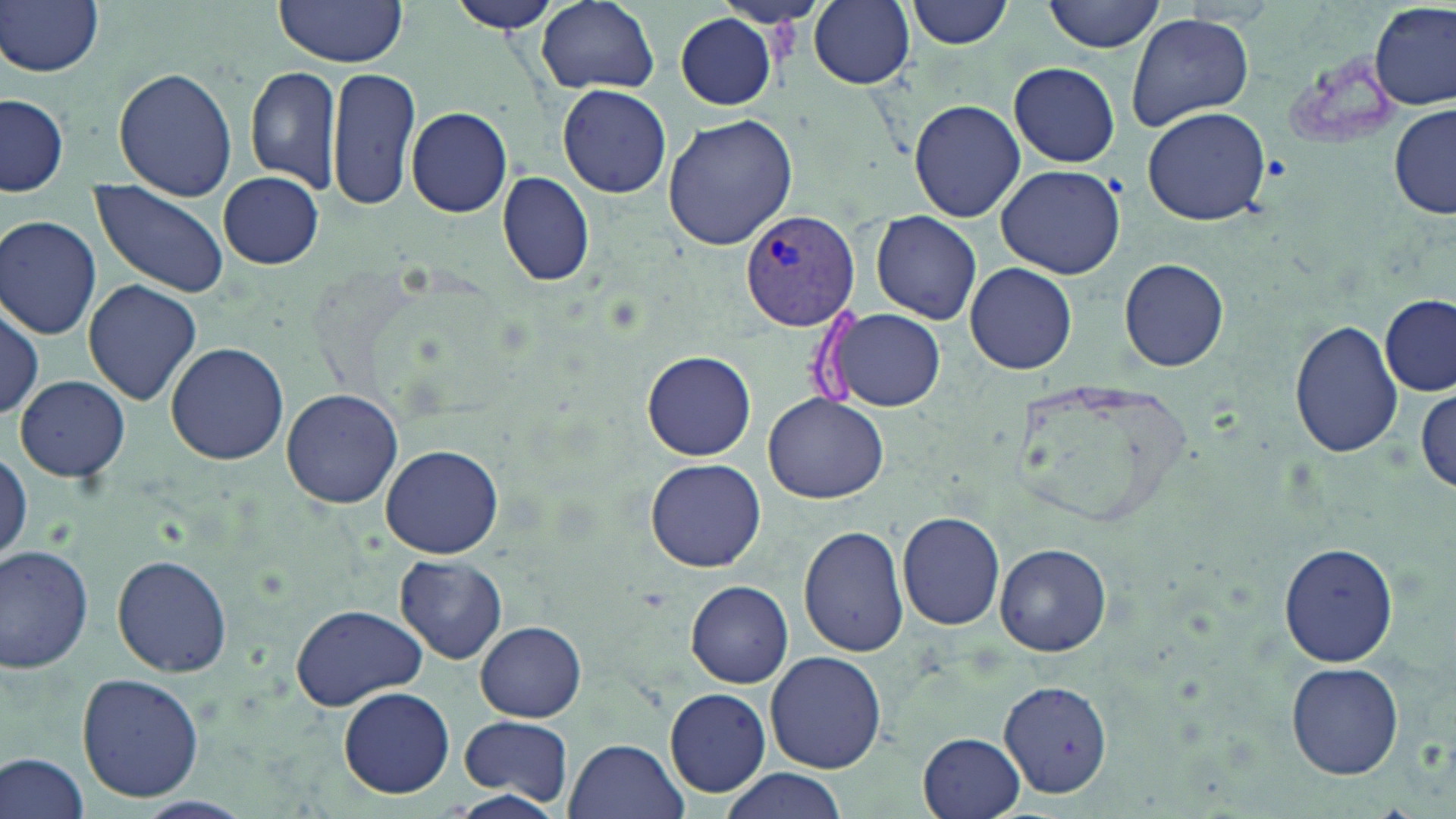
Summary:
  - Coordinate format: approximate bounding boxes as (x1,y1)-(x2,y2) corner pairs in pixels
  - Plasmodium vivax-infected red blood cell locations: (739,213)-(856,331)
  - Uninfected red blood cell locations: (271,0)-(409,69), (444,0)-(566,34), (536,0)-(660,94), (808,0)-(915,89), (906,0)-(1015,48), (1044,0)-(1166,51), (1,1)-(106,77), (1371,3)-(1454,112), (1127,12)-(1255,131), (676,13)-(776,110), (1008,62)-(1120,167), (114,65)-(237,201), (246,66)-(342,190), (328,66)-(422,213), (558,84)-(671,199), (1,92)-(70,194), (909,98)-(1026,222), (1140,105)-(1272,226), (1390,105)-(1456,221), (406,106)-(514,218), (662,113)-(799,251), (995,164)-(1126,279), (217,171)-(324,268), (495,172)-(596,287), (90,181)-(230,297), (868,213)-(987,324), (0,214)-(103,338), (1119,256)-(1229,372), (965,263)-(1077,376), (81,280)-(201,407), (1380,295)-(1455,395), (1,300)-(43,418), (828,306)-(947,414), (1290,316)-(1404,459), (164,341)-(290,465), (641,351)-(757,461), (15,374)-(130,483), (280,386)-(403,508), (1415,388)-(1455,493), (762,395)-(892,504), (379,443)-(504,559), (645,459)-(766,571), (897,511)-(1007,631), (798,525)-(909,656), (1279,541)-(1399,667), (0,543)-(98,676), (994,543)-(1111,656), (113,554)-(232,677), (393,555)-(508,664), (685,580)-(794,688), (289,603)-(428,710), (476,621)-(587,721), (766,650)-(886,772), (1287,661)-(1403,780), (76,673)-(205,802), (997,678)-(1114,799), (338,685)-(455,800), (665,688)-(772,798), (459,713)-(574,807), (919,731)-(1025,817), (565,737)-(688,819), (0,751)-(93,819), (717,769)-(849,819), (448,789)-(564,819)
  - Slide-level diagnosis: Plasmodium vivax
  - Stain: May-Grünwald-Giemsa
  - Preparation: thin blood film
  - Modality: optical microscopy
  - Image size: 1456×819 pixels
  - Magnification: 1000x
  - Field of view: single